Comment on the morphology of the red blood cells.
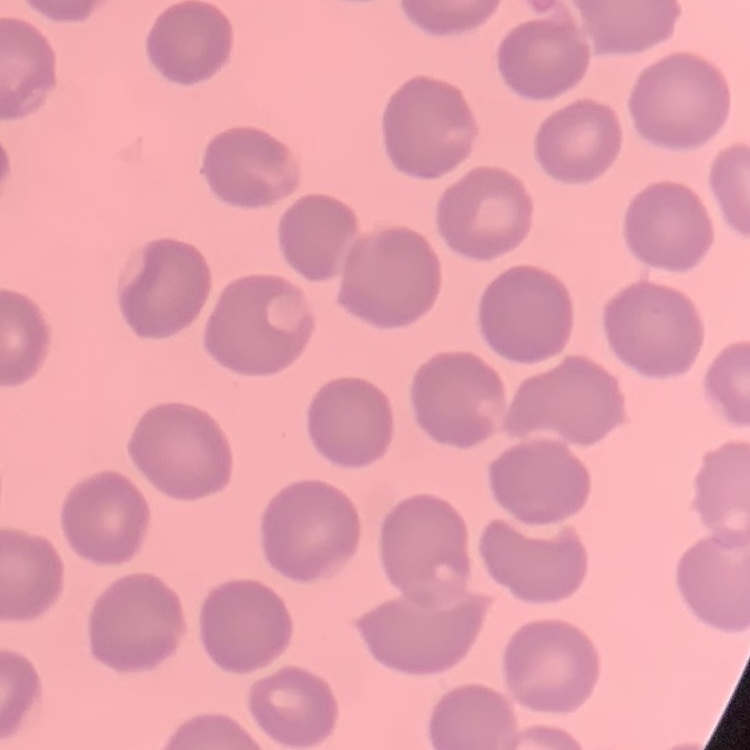

They show no rouleaux formation.

preparation: thin blood smear
image_type: square crop of a larger photomicrograph
stain: Field's or Giemsa